Classify this cell by malaria status.
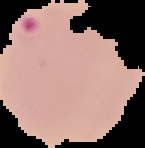

It is parasitized.

image_size: 145×148 pixels
preparation: thin blood smear
image_type: cell region segmented out of the field of view; surrounding area masked to black